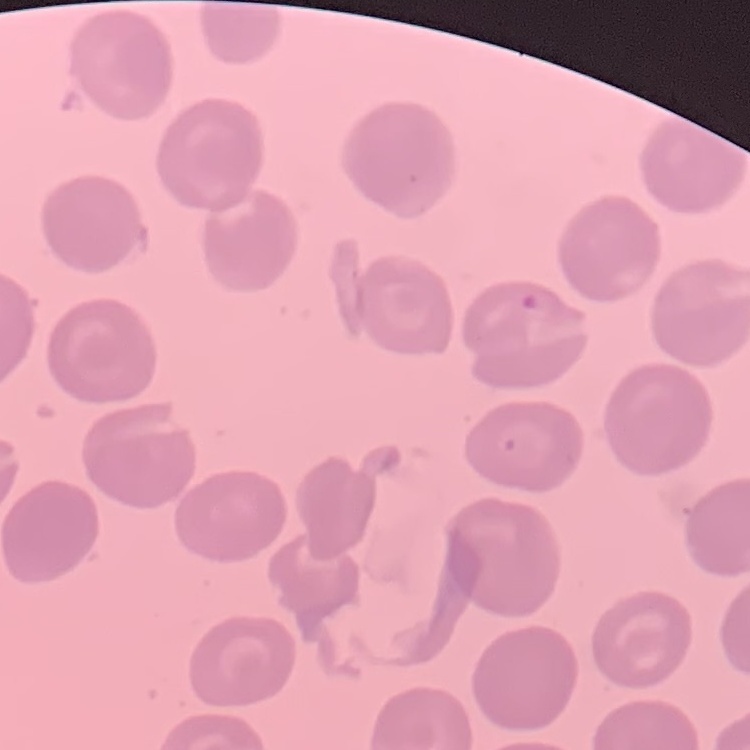
erythrocyte morphology = no rouleaux formation
image type = one tile cut from a larger photomicrograph
preparation = thin blood film
stain = Field's or Giemsa